Locate every Plasmodium parasite and every leukocyte.
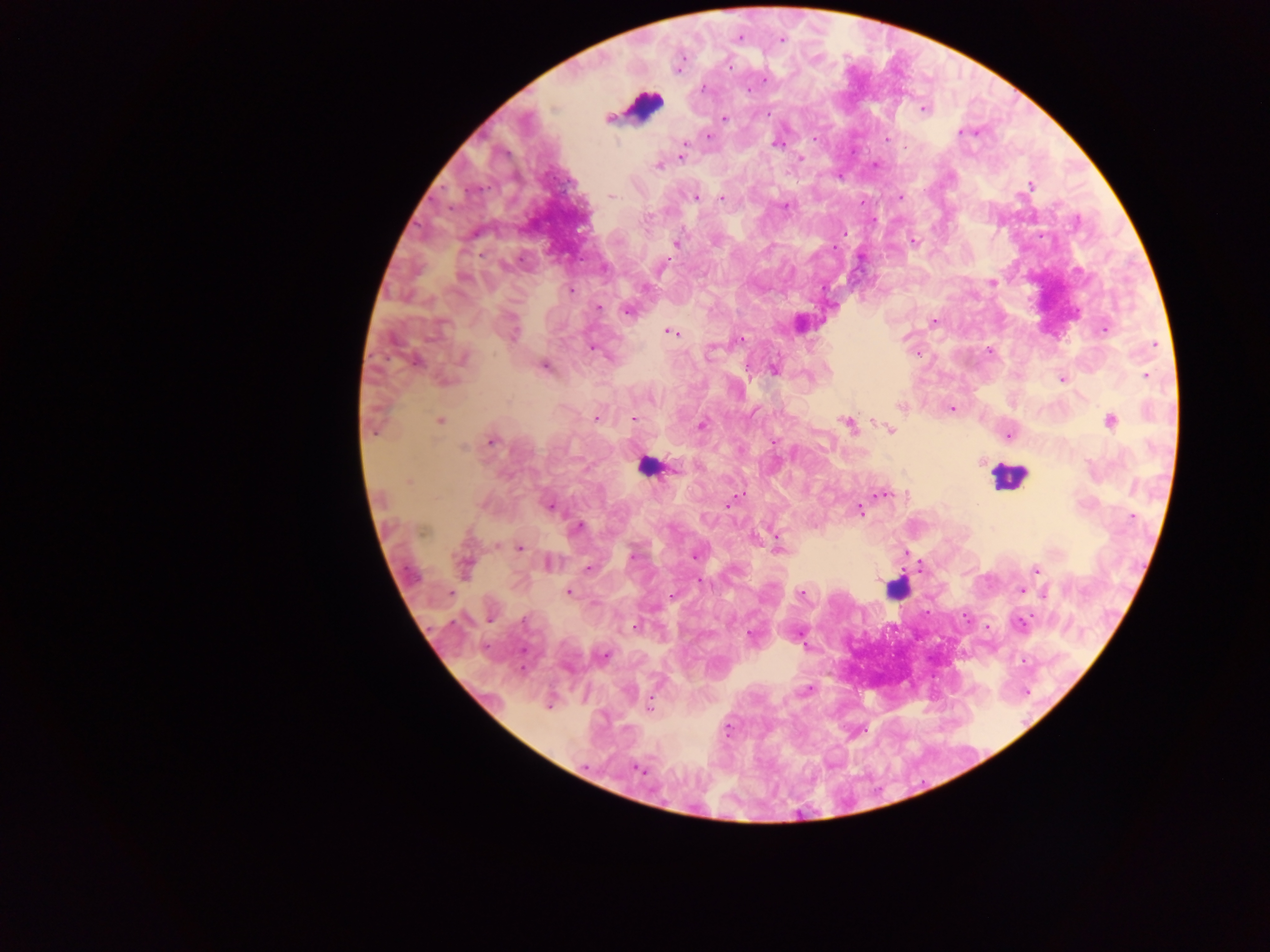
Approximate centers as [x, y] in pixels.
Plasmodium parasites: [739, 37], [781, 40], [764, 81], [703, 87], [923, 109], [724, 118], [960, 132], [709, 136], [887, 139], [777, 144], [685, 146], [683, 152], [800, 159], [658, 166], [1031, 184], [611, 196], [696, 196], [900, 197], [721, 198], [784, 206], [913, 240], [676, 244], [661, 268], [464, 279], [992, 282], [571, 291], [599, 308], [627, 310], [934, 321], [1104, 330], [513, 332], [670, 332], [740, 340], [591, 349], [989, 350], [709, 353], [918, 354], [463, 358], [416, 362], [544, 366], [774, 370], [1146, 375], [1062, 379], [900, 406], [952, 409], [597, 418], [634, 419], [1111, 420], [439, 421], [848, 424], [702, 426], [891, 430], [1008, 435], [491, 441], [773, 443], [464, 447], [408, 482], [883, 494], [736, 497], [732, 501], [549, 507], [859, 510], [1132, 517], [578, 527], [778, 545], [520, 547], [632, 556], [694, 556], [549, 563], [464, 566], [588, 569], [1037, 569], [700, 581], [1021, 590], [568, 592], [801, 594], [1045, 594], [491, 617], [524, 620], [1021, 622], [635, 626], [751, 635], [800, 638], [604, 656], [808, 690], [549, 705], [650, 705], [636, 769].
Leukocytes: [642, 106], [648, 466], [1006, 476], [897, 589].

Mobile-phone photograph taken through the microscope. Single field of view. Collected in Ghana. Image is 1270×952 pixels. Thick blood smear.